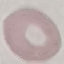

{
  "result": "negative for malaria parasites",
  "preparation": "thin blood film",
  "image_type": "automatically extracted cell patch, resized to 64 × 64 pixels",
  "stain": "Giemsa",
  "capture": "smartphone through the microscope eyepiece"
}